Outline each Plasmodium falciparum-infected red blood cell.
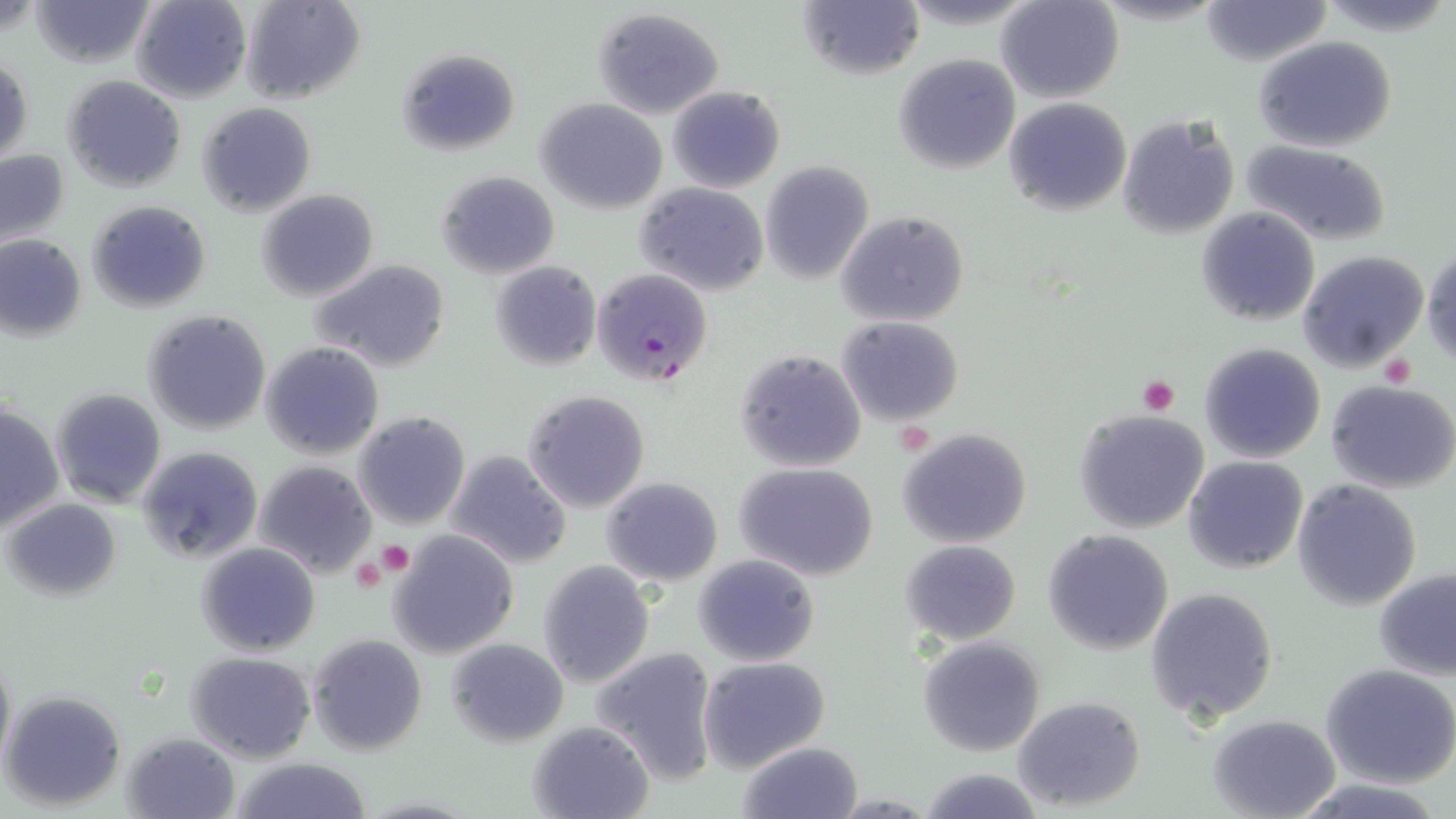
Approximate bounding boxes as named x1/y1/x2/y2 corners in pixels.
Plasmodium falciparum-infected red blood cells: (x1=590, y1=267, x2=713, y2=388).

{
  "slide_level_diagnosis": "Plasmodium falciparum",
  "stain": "May-Grünwald-Giemsa",
  "uninfected_red_blood_cell_locations": "approximate bounding boxes as named x1/y1/x2/y2 corners in pixels: (x1=31, y1=0, x2=156, y2=68), (x1=130, y1=0, x2=251, y2=104), (x1=242, y1=0, x2=365, y2=104), (x1=997, y1=0, x2=1125, y2=102), (x1=1198, y1=1, x2=1333, y2=66), (x1=798, y1=2, x2=923, y2=81), (x1=592, y1=7, x2=725, y2=119), (x1=1255, y1=36, x2=1396, y2=153), (x1=396, y1=49, x2=520, y2=156), (x1=1, y1=54, x2=33, y2=164), (x1=893, y1=54, x2=1020, y2=173), (x1=63, y1=76, x2=187, y2=193), (x1=667, y1=85, x2=785, y2=193), (x1=1002, y1=96, x2=1132, y2=217), (x1=535, y1=98, x2=667, y2=213), (x1=198, y1=103, x2=315, y2=216), (x1=1115, y1=114, x2=1241, y2=241), (x1=1241, y1=141, x2=1392, y2=244), (x1=0, y1=149, x2=71, y2=248), (x1=760, y1=162, x2=875, y2=283), (x1=435, y1=171, x2=559, y2=278), (x1=635, y1=183, x2=769, y2=296), (x1=255, y1=189, x2=379, y2=301), (x1=88, y1=200, x2=212, y2=312), (x1=1196, y1=207, x2=1321, y2=326), (x1=836, y1=211, x2=970, y2=327), (x1=95, y1=226, x2=228, y2=371), (x1=0, y1=234, x2=87, y2=341), (x1=1422, y1=248, x2=1456, y2=365), (x1=1298, y1=250, x2=1428, y2=373), (x1=312, y1=258, x2=451, y2=372), (x1=488, y1=260, x2=602, y2=371), (x1=142, y1=310, x2=271, y2=435), (x1=836, y1=316, x2=965, y2=425), (x1=260, y1=341, x2=385, y2=459), (x1=1198, y1=342, x2=1326, y2=463), (x1=733, y1=350, x2=867, y2=473), (x1=1128, y1=375, x2=1190, y2=414), (x1=1326, y1=379, x2=1456, y2=494), (x1=51, y1=388, x2=168, y2=508), (x1=523, y1=389, x2=652, y2=513), (x1=1, y1=403, x2=65, y2=533), (x1=1074, y1=408, x2=1211, y2=535), (x1=353, y1=411, x2=472, y2=530), (x1=898, y1=427, x2=1032, y2=547), (x1=137, y1=446, x2=265, y2=566), (x1=444, y1=450, x2=572, y2=570), (x1=1183, y1=455, x2=1309, y2=574), (x1=252, y1=459, x2=377, y2=579), (x1=735, y1=462, x2=882, y2=582), (x1=601, y1=477, x2=724, y2=586), (x1=1292, y1=480, x2=1421, y2=608), (x1=5, y1=498, x2=120, y2=600), (x1=1043, y1=529, x2=1174, y2=653), (x1=390, y1=530, x2=520, y2=660), (x1=899, y1=540, x2=1022, y2=644), (x1=196, y1=542, x2=321, y2=657), (x1=693, y1=553, x2=821, y2=669), (x1=537, y1=561, x2=655, y2=688), (x1=1374, y1=568, x2=1456, y2=680), (x1=1145, y1=586, x2=1279, y2=722), (x1=306, y1=632, x2=429, y2=757), (x1=916, y1=636, x2=1046, y2=757), (x1=445, y1=637, x2=569, y2=747), (x1=0, y1=647, x2=14, y2=777), (x1=590, y1=647, x2=720, y2=784), (x1=185, y1=651, x2=316, y2=762), (x1=698, y1=656, x2=831, y2=774), (x1=1322, y1=663, x2=1456, y2=789), (x1=1, y1=689, x2=126, y2=810), (x1=1012, y1=694, x2=1145, y2=812), (x1=1207, y1=714, x2=1342, y2=819), (x1=527, y1=720, x2=657, y2=818), (x1=121, y1=732, x2=242, y2=819), (x1=736, y1=740, x2=865, y2=818), (x1=229, y1=757, x2=375, y2=818), (x1=918, y1=767, x2=1044, y2=818), (x1=1287, y1=778, x2=1450, y2=819)",
  "magnification": "1000x",
  "preparation": "thin blood smear",
  "platelet_locations": "approximate bounding boxes as named x1/y1/x2/y2 corners in pixels: (x1=1378, y1=353, x2=1416, y2=386), (x1=1134, y1=375, x2=1181, y2=416), (x1=375, y1=540, x2=415, y2=579), (x1=352, y1=556, x2=386, y2=592)",
  "modality": "optical microscopy",
  "image_size": "1456×819 pixels",
  "field_of_view": "one of a larger specimen"
}